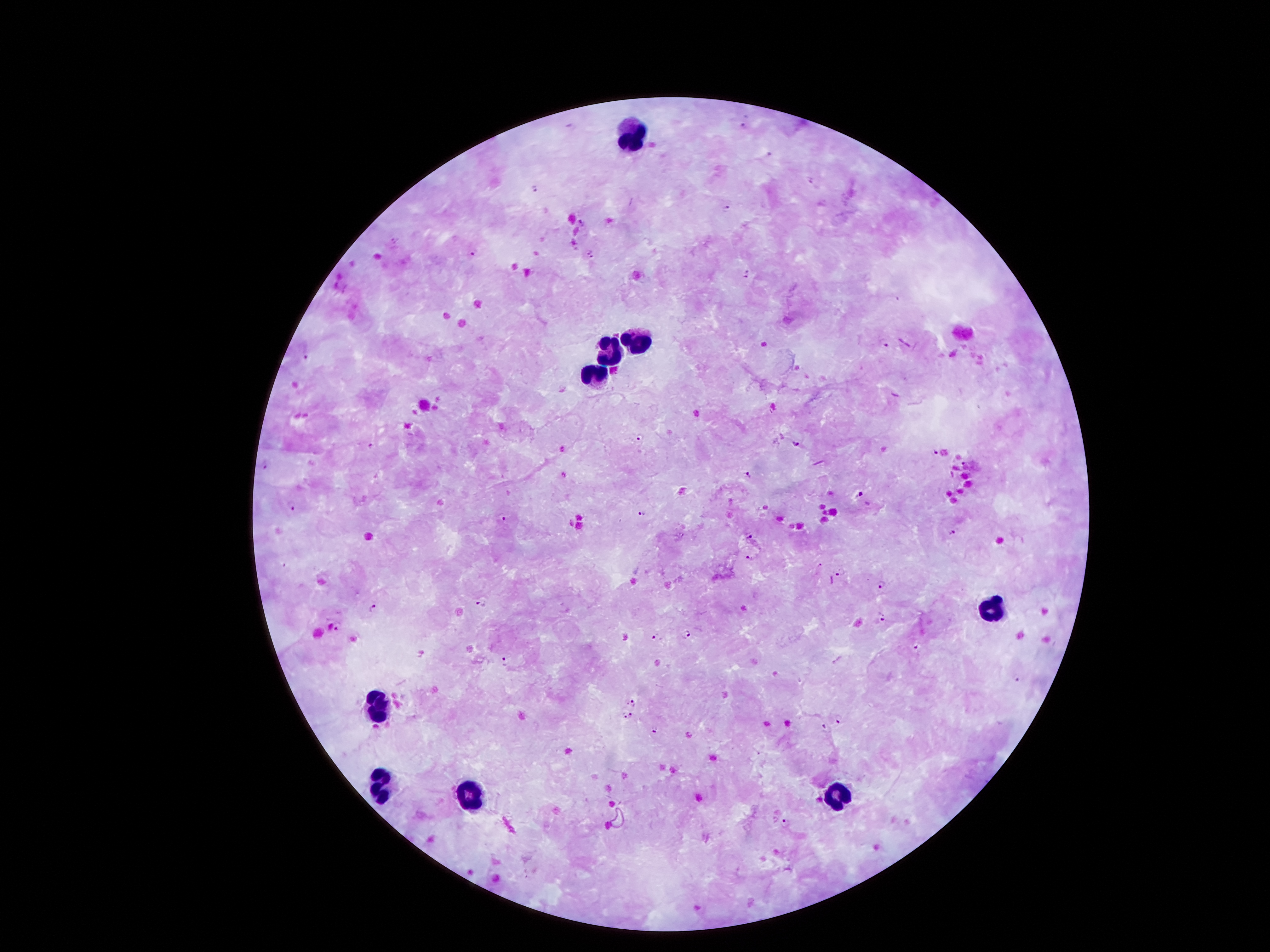
Approximate centers as [x, y] in pixels.
Summary:
  - Malaria parasite locations: [745, 125], [768, 152], [535, 188], [727, 207], [580, 223], [395, 240], [589, 251], [475, 252], [592, 259], [748, 273], [898, 301], [885, 343], [306, 356], [641, 437], [371, 445], [794, 445], [935, 453], [266, 465], [749, 475], [861, 494], [291, 504], [642, 514], [503, 516], [952, 533], [748, 536], [749, 558], [821, 564], [842, 571], [883, 587], [481, 606], [372, 607], [882, 619], [337, 625], [687, 632], [656, 635], [916, 649], [507, 660], [1019, 679], [632, 702], [628, 716], [839, 718], [654, 729], [824, 729], [787, 823]
  - Leukocyte locations: [632, 134], [638, 336], [611, 351], [594, 376], [987, 613], [378, 704], [382, 790], [470, 790], [837, 796]
  - Magnification: 100x
  - Capture: smartphone through the microscope eyepiece
  - Field of view: single
  - Image size: 1270×952 pixels
  - Stain: Giemsa
  - Patient malaria status: positive for Plasmodium falciparum
  - Preparation: thick blood film